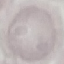 Malaria status: uninfected. Giemsa stain. Thin blood film. Cell patch, automatically extracted from a larger field of view and resized to 64 × 64 pixels. Photographed with a smartphone camera at the microscope eyepiece.